Assess this cell for malaria.
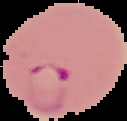
Parasitized.

image size = 127×121 pixels
preparation = thin blood smear
image type = segmented cell region with the area outside set to black